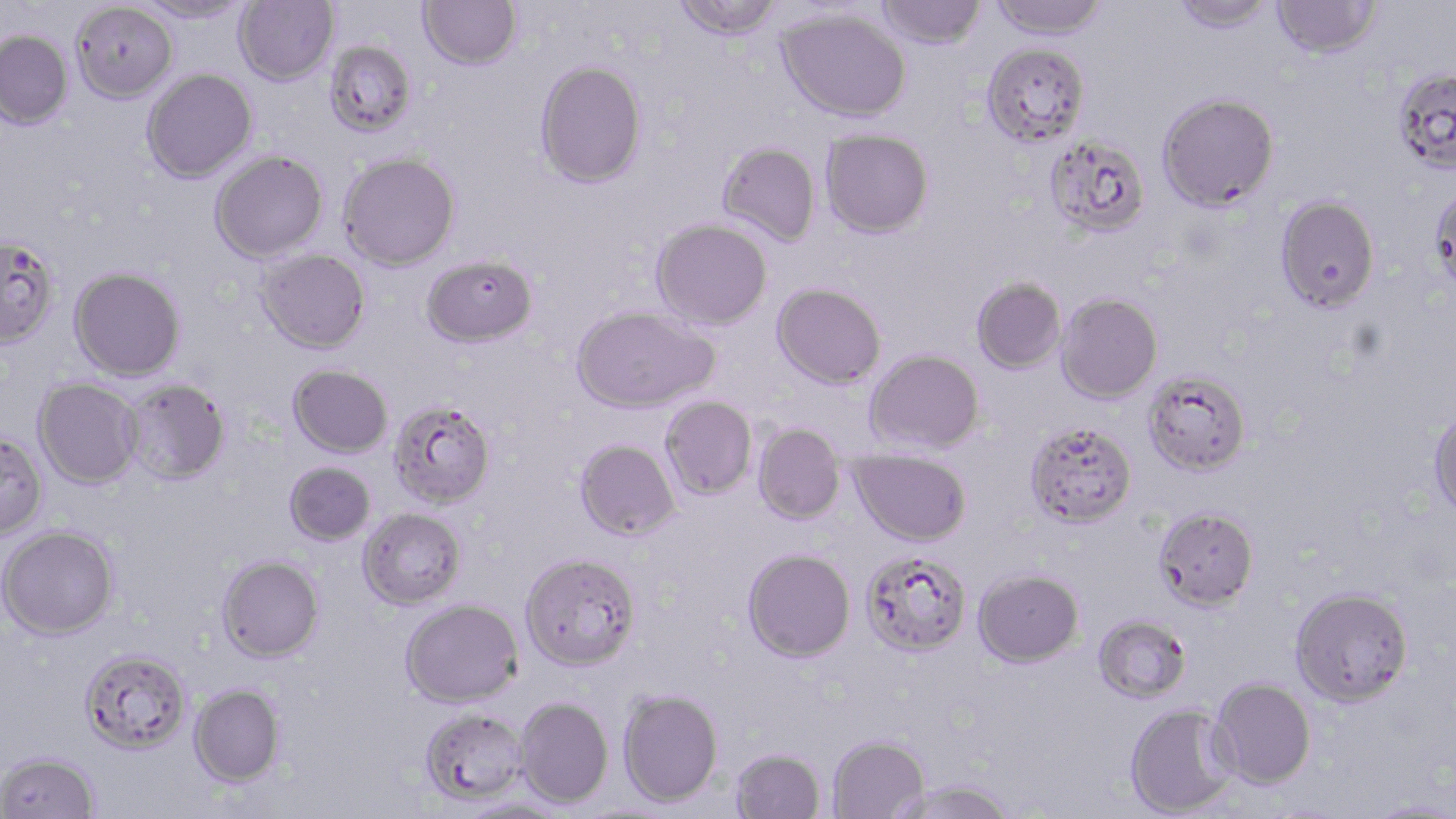
Summary:
  - Coordinate format: approximate bounding boxes as [x1, y1, x2, y2] in pixels
  - Uninfected red blood cell locations: [138, 0, 253, 24], [234, 0, 339, 85], [418, 0, 522, 70], [672, 0, 785, 41], [876, 0, 986, 49], [989, 0, 1110, 41], [1169, 0, 1279, 34], [1271, 0, 1382, 58], [71, 2, 177, 103], [776, 8, 911, 122], [0, 29, 73, 129], [324, 40, 417, 137], [982, 42, 1090, 146], [535, 59, 647, 187], [1392, 67, 1456, 173], [141, 68, 257, 183], [1157, 92, 1279, 211], [820, 129, 934, 238], [1043, 134, 1151, 239], [717, 142, 821, 246], [209, 150, 328, 263], [338, 151, 460, 271], [1430, 183, 1456, 297], [1275, 195, 1381, 313], [651, 218, 772, 330], [0, 236, 59, 347], [255, 249, 370, 354], [421, 254, 538, 347], [69, 267, 186, 380], [970, 277, 1066, 374], [772, 283, 886, 389], [1056, 292, 1162, 404], [570, 306, 719, 414], [865, 348, 984, 454], [288, 364, 393, 458], [1143, 371, 1251, 476], [33, 379, 142, 489], [122, 379, 231, 484], [660, 396, 757, 500], [389, 399, 497, 509], [1428, 406, 1456, 517], [1024, 420, 1137, 528], [753, 423, 846, 524], [0, 432, 47, 538], [574, 439, 681, 541], [850, 448, 971, 546], [283, 461, 376, 545], [1153, 506, 1259, 610], [358, 507, 466, 609], [0, 525, 119, 639], [742, 548, 856, 662], [860, 551, 972, 657], [519, 552, 641, 671], [217, 555, 324, 662], [973, 568, 1084, 667], [1290, 586, 1414, 707], [401, 598, 523, 707], [1093, 614, 1192, 703], [79, 647, 191, 754], [1210, 677, 1316, 788], [189, 683, 285, 787], [618, 689, 723, 807], [515, 696, 613, 808], [1124, 704, 1238, 817], [420, 707, 528, 805], [827, 735, 928, 819], [730, 747, 825, 818], [0, 751, 100, 818], [889, 780, 1017, 819], [458, 798, 570, 819], [1363, 798, 1456, 818]
  - Slide-level diagnosis: Plasmodium falciparum
  - Image size: 1456×819 pixels
  - Magnification: 1000x
  - Stain: May-Grünwald-Giemsa
  - Preparation: thin blood film
  - Modality: light microscopy
  - Field of view: single